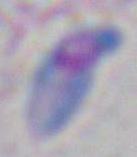

Summary:
  - Identification: Toxoplasma gondii
  - Modality: photomicrograph
  - Magnification: 1000x